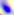
Photomicrograph. Toxoplasma gondii is shown. Captured at 400x magnification.